Locate platelets.
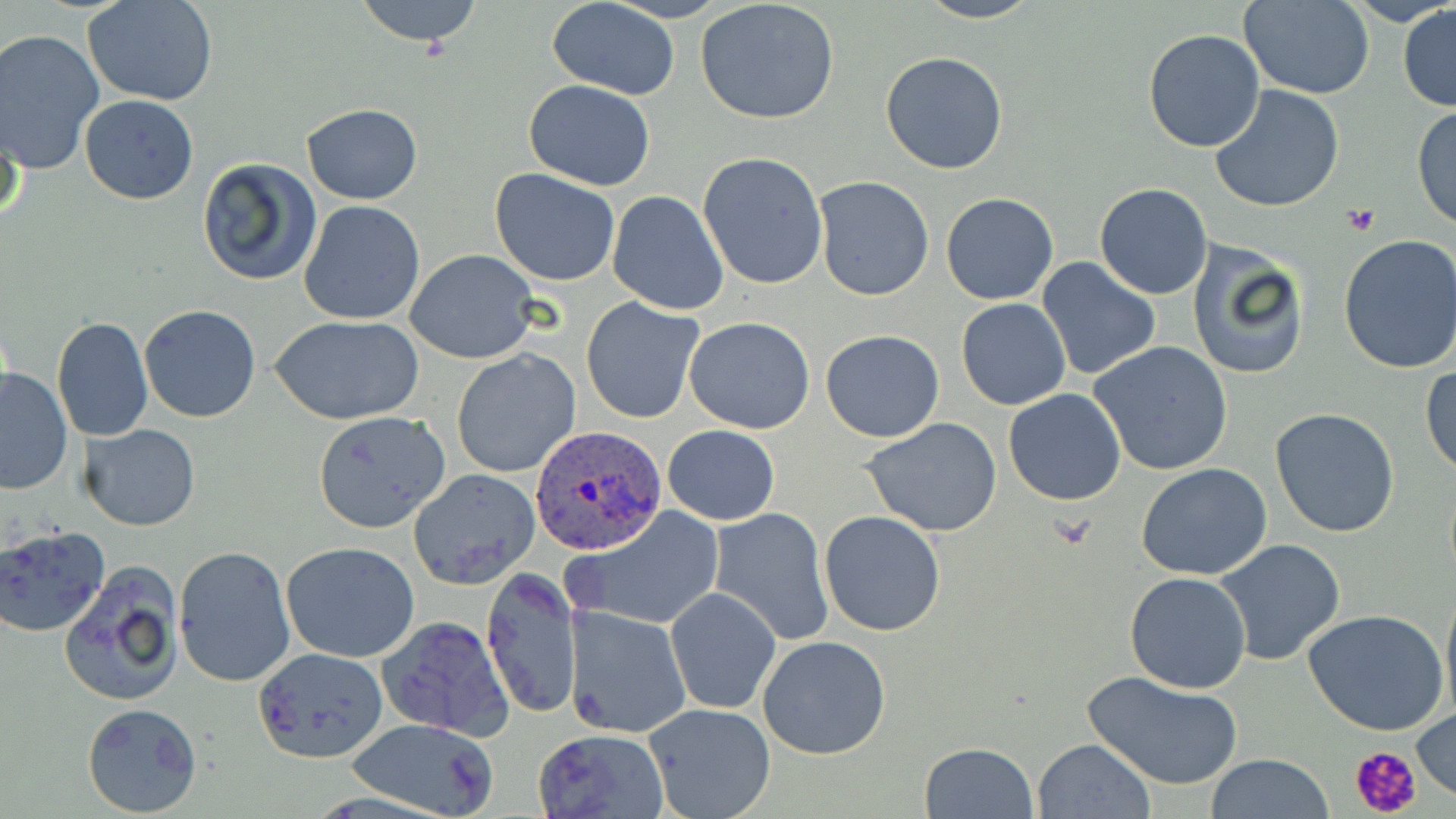
Approximate bounding boxes as named x1/y1/x2/y2 corners in pixels.
Platelets: (x1=1342, y1=205, x2=1381, y2=235), (x1=1349, y1=744, x2=1424, y2=817).

Plasmodium ovale-infected red blood cell locations: (x1=531, y1=426, x2=665, y2=554). Uninfected red blood cell locations: (x1=84, y1=0, x2=219, y2=107), (x1=353, y1=0, x2=487, y2=50), (x1=547, y1=0, x2=681, y2=98), (x1=914, y1=0, x2=1045, y2=24), (x1=1239, y1=0, x2=1373, y2=98), (x1=1345, y1=0, x2=1455, y2=27), (x1=695, y1=1, x2=842, y2=124), (x1=1398, y1=3, x2=1456, y2=112), (x1=1143, y1=28, x2=1266, y2=153), (x1=0, y1=29, x2=104, y2=174), (x1=879, y1=52, x2=1009, y2=175), (x1=523, y1=80, x2=655, y2=190), (x1=1210, y1=85, x2=1347, y2=214), (x1=80, y1=94, x2=198, y2=204), (x1=300, y1=103, x2=422, y2=203), (x1=1412, y1=104, x2=1456, y2=230), (x1=0, y1=110, x2=24, y2=233), (x1=697, y1=151, x2=829, y2=290), (x1=196, y1=157, x2=323, y2=287), (x1=490, y1=168, x2=620, y2=285), (x1=812, y1=176, x2=934, y2=302), (x1=1094, y1=183, x2=1214, y2=299), (x1=606, y1=190, x2=729, y2=315), (x1=941, y1=192, x2=1058, y2=306), (x1=297, y1=199, x2=425, y2=326), (x1=1335, y1=234, x2=1456, y2=376), (x1=1187, y1=240, x2=1313, y2=381), (x1=406, y1=248, x2=539, y2=364), (x1=1037, y1=258, x2=1161, y2=379), (x1=581, y1=296, x2=705, y2=424), (x1=955, y1=298, x2=1072, y2=411), (x1=138, y1=305, x2=262, y2=423), (x1=268, y1=315, x2=425, y2=424), (x1=685, y1=316, x2=816, y2=433), (x1=52, y1=317, x2=154, y2=442), (x1=819, y1=330, x2=945, y2=442), (x1=1088, y1=340, x2=1234, y2=476), (x1=451, y1=349, x2=580, y2=479), (x1=1421, y1=363, x2=1455, y2=478), (x1=0, y1=367, x2=73, y2=494), (x1=1004, y1=389, x2=1127, y2=507), (x1=1270, y1=407, x2=1400, y2=539), (x1=313, y1=411, x2=453, y2=535), (x1=859, y1=418, x2=1005, y2=537), (x1=80, y1=424, x2=200, y2=531), (x1=664, y1=424, x2=779, y2=526), (x1=1136, y1=461, x2=1272, y2=581), (x1=407, y1=468, x2=541, y2=590), (x1=566, y1=506, x2=724, y2=632), (x1=710, y1=508, x2=835, y2=646), (x1=819, y1=511, x2=946, y2=636), (x1=0, y1=526, x2=110, y2=639), (x1=1213, y1=538, x2=1346, y2=667), (x1=281, y1=542, x2=422, y2=663), (x1=174, y1=545, x2=297, y2=690), (x1=59, y1=562, x2=184, y2=708), (x1=480, y1=566, x2=580, y2=720), (x1=1123, y1=572, x2=1252, y2=695), (x1=1440, y1=579, x2=1456, y2=722), (x1=664, y1=585, x2=782, y2=715), (x1=564, y1=604, x2=690, y2=740), (x1=1303, y1=609, x2=1450, y2=737), (x1=377, y1=614, x2=515, y2=742), (x1=757, y1=635, x2=892, y2=759), (x1=252, y1=648, x2=387, y2=763), (x1=1082, y1=669, x2=1244, y2=790), (x1=81, y1=702, x2=203, y2=817), (x1=644, y1=703, x2=776, y2=819), (x1=1413, y1=705, x2=1455, y2=798), (x1=346, y1=718, x2=503, y2=817), (x1=532, y1=727, x2=670, y2=819), (x1=1032, y1=738, x2=1156, y2=818), (x1=919, y1=742, x2=1038, y2=818), (x1=1205, y1=755, x2=1336, y2=817). Slide-level diagnosis: Plasmodium ovale. 1000x magnification. Light microscopy. Thin blood smear. May-Grünwald-Giemsa-stained preparation. Image is 1456×819 pixels. Single field of view.